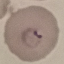

Summary:
  - Malaria status: parasitized
  - Preparation: thin blood smear
  - Image type: cell patch, automatically extracted from a larger field of view and resized to 64 × 64 pixels
  - Stain: Giemsa
  - Capture: smartphone through the microscope eyepiece